Describe the morphology of the red blood cells.
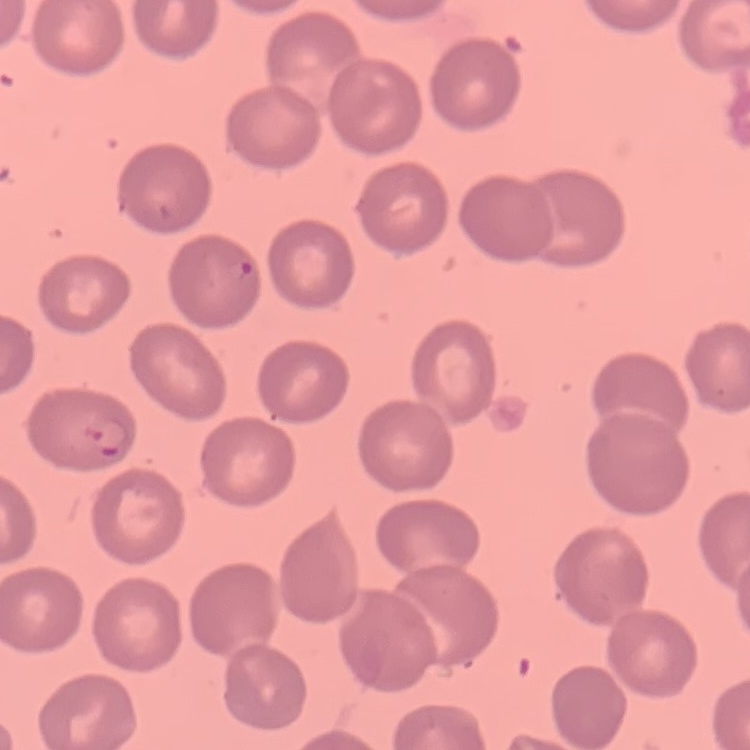
No rouleaux formation.

Summary:
  - Preparation: thin peripheral smear
  - Image type: square crop of a larger photomicrograph
  - Stain: Field's or Giemsa